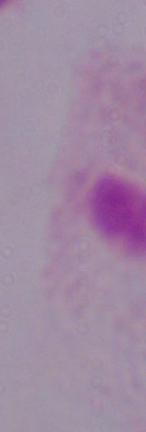

1000x magnification. A trichomonad is shown. Micrograph.